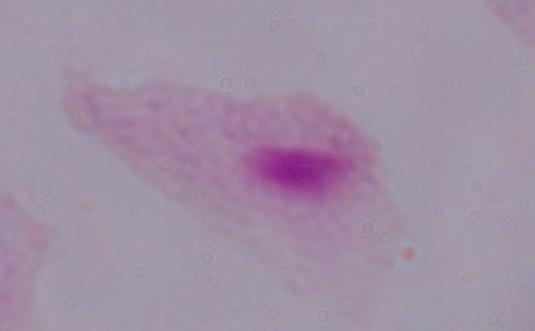 1000x magnification. Photomicrograph. A trichomonad is seen.